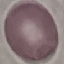

Summary:
  - Result: negative for malaria parasites
  - Capture: smartphone camera at the microscope eyepiece
  - Preparation: thin smear
  - Stain: Giemsa
  - Image type: automatically extracted cell patch, resized to 64 × 64 pixels